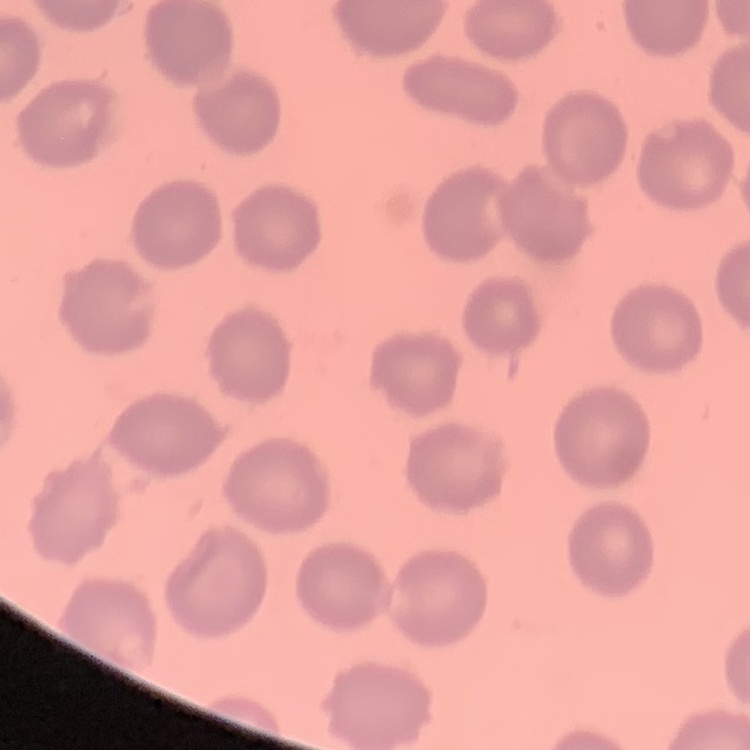

Summary:
  - Erythrocyte morphology: no rouleaux formation
  - Stain: Field's or Giemsa
  - Image type: square crop of a larger photomicrograph
  - Preparation: thin blood film